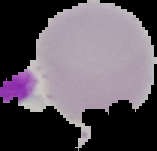

Summary:
  - Image type: segmented cell region with the area outside set to black
  - Preparation: thin blood smear
  - Image size: 157×151 pixels
  - Malaria status: uninfected